State the blood parasite species.
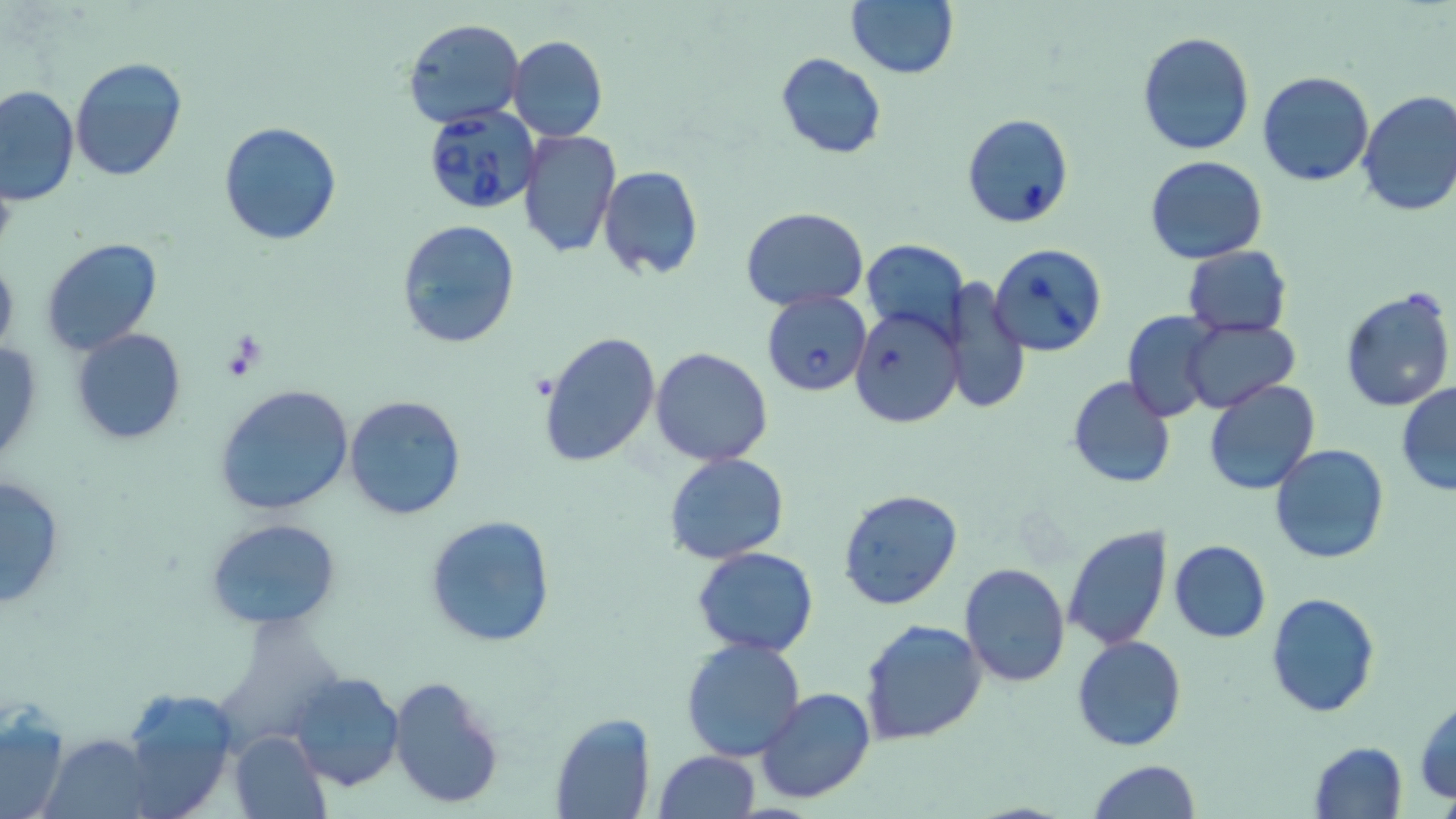
Babesia divergens.

stain = May-Grünwald-Giemsa
modality = light microscopy
field of view = single
Babesia divergens-infected red blood cell locations = approximate bounding boxes as (x1,y1)-(x2,y2) corner pairs in pixels: (420,104)-(539,215), (961,112)-(1074,229), (989,243)-(1107,356), (762,290)-(872,397), (848,307)-(961,427)
magnification = 1000x
image size = 1456×819 pixels
uninfected red blood cell locations = approximate bounding boxes as (x1,y1)-(x2,y2) corner pairs in pixels: (845,0)-(959,80), (402,17)-(524,128), (1137,31)-(1255,157), (509,35)-(608,143), (775,52)-(887,160), (69,57)-(188,181), (1257,71)-(1375,187), (0,85)-(79,206), (1356,90)-(1456,216), (218,121)-(342,247), (518,129)-(622,259), (1144,155)-(1268,264), (598,166)-(704,279), (741,207)-(868,311), (395,219)-(521,350), (40,236)-(163,356), (862,237)-(966,341), (1182,245)-(1291,338), (0,253)-(19,364), (944,278)-(1029,417), (1340,286)-(1456,414), (1123,312)-(1221,421), (1182,317)-(1300,414), (72,328)-(187,444), (538,330)-(662,471), (0,337)-(44,469), (650,346)-(776,466), (1068,376)-(1173,489), (1203,378)-(1321,496), (1395,383)-(1456,496), (214,384)-(356,518), (344,393)-(467,522), (1270,444)-(1391,565), (662,453)-(789,565), (1,472)-(68,612), (837,488)-(963,610), (424,515)-(558,650), (204,517)-(340,629), (1062,527)-(1170,650), (1168,540)-(1271,642), (692,546)-(820,658), (959,562)-(1069,686), (1266,592)-(1380,718), (861,619)-(987,745), (1072,636)-(1186,752), (681,637)-(805,761), (287,671)-(406,792), (388,675)-(506,809), (755,685)-(875,804), (116,687)-(237,816), (1414,699)-(1456,802), (0,705)-(70,819), (550,712)-(656,819), (228,730)-(329,819), (46,732)-(154,818), (1307,740)-(1408,819), (652,750)-(760,819), (1086,758)-(1199,819)
preparation = thin blood film